Describe the morphology of the red blood cells.
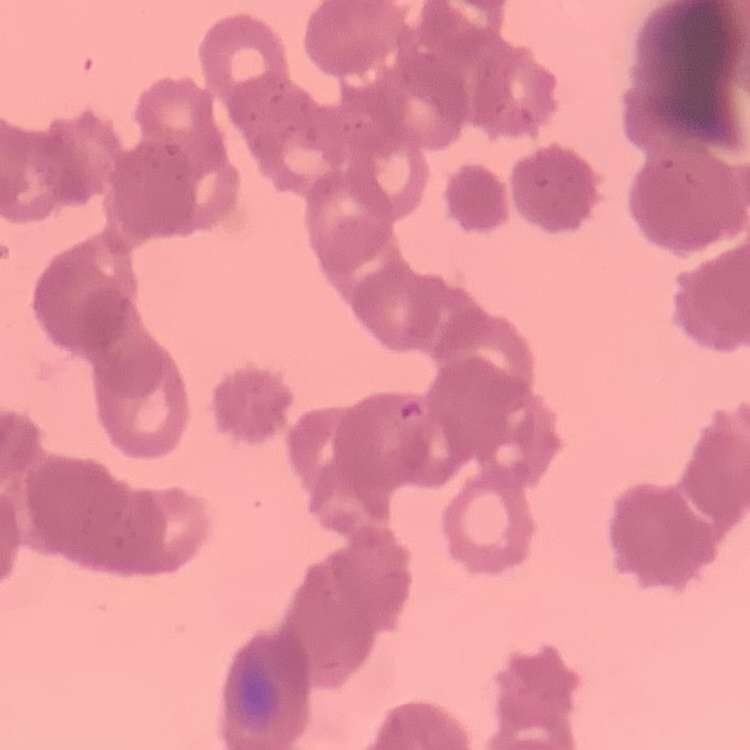
Rouleaux formation.

Summary:
  - Preparation: thin peripheral smear
  - Stain: Field's or Giemsa
  - Image type: square crop of a larger photomicrograph